Give the position of every Plasmodium parasite.
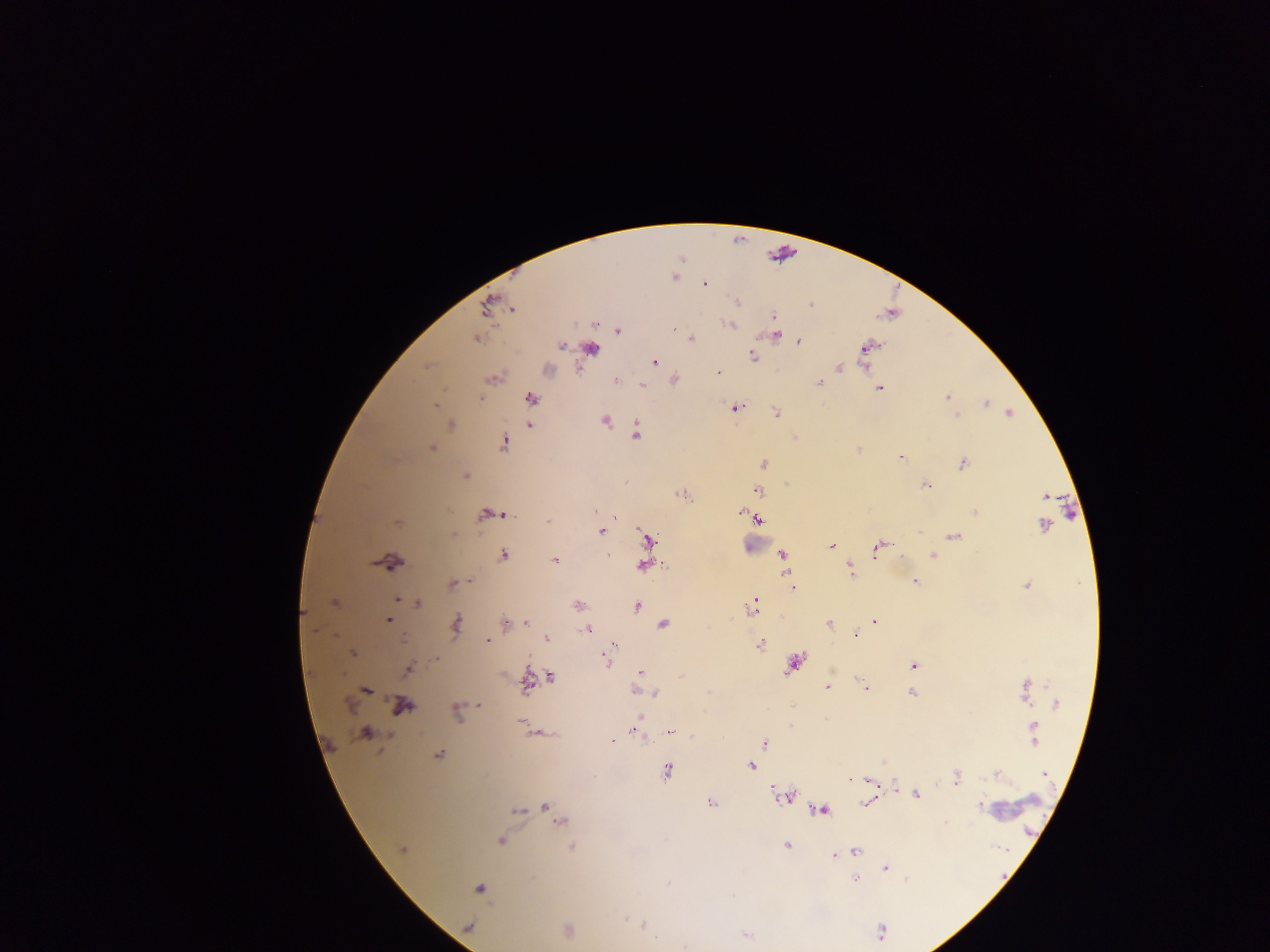

Approximate centers as {x, y} in pixels.
Plasmodium parasites: {703, 283}, {736, 304}, {812, 308}, {773, 315}, {730, 326}, {673, 327}, {775, 334}, {691, 338}, {477, 339}, {796, 339}, {798, 342}, {561, 345}, {865, 347}, {590, 348}, {861, 354}, {753, 355}, {654, 362}, {865, 364}, {839, 368}, {719, 373}, {614, 379}, {818, 383}, {642, 385}, {879, 388}, {946, 397}, {480, 398}, {530, 398}, {987, 403}, {435, 405}, {735, 408}, {776, 413}, {1009, 413}, {952, 414}, {957, 414}, {606, 420}, {528, 424}, {637, 434}, {504, 440}, {432, 448}, {858, 448}, {900, 456}, {764, 463}, {962, 464}, {465, 475}, {926, 484}, {757, 490}, {1044, 496}, {595, 510}, {740, 512}, {973, 512}, {482, 513}, {504, 515}, {548, 519}, {758, 519}, {1042, 526}, {599, 531}, {920, 532}, {953, 536}, {646, 538}, {832, 546}, {877, 549}, {608, 553}, {503, 554}, {782, 554}, {932, 554}, {554, 560}, {388, 563}, {642, 566}, {850, 567}, {787, 575}, {916, 581}, {451, 582}, {469, 582}, {1025, 585}, {794, 590}, {397, 600}, {417, 603}, {576, 605}, {754, 606}, {638, 607}, {749, 610}, {304, 613}, {388, 620}, {875, 621}, {503, 622}, {527, 624}, {662, 624}, {829, 624}, {455, 625}, {588, 629}, {855, 635}, {546, 638}, {486, 640}, {761, 645}, {352, 654}, {606, 660}, {912, 665}, {407, 669}, {832, 669}, {640, 672}, {527, 675}, {639, 675}, {552, 676}, {680, 677}, {526, 684}, {1024, 685}, {866, 686}, {828, 687}, {367, 690}, {634, 691}, {655, 692}, {910, 692}, {1026, 701}, {480, 704}, {791, 705}, {399, 706}, {455, 708}, {638, 716}, {520, 721}, {790, 725}, {1034, 725}, {634, 729}, {366, 732}, {671, 733}, {636, 734}, {612, 740}, {1037, 740}, {1035, 742}, {765, 743}, {438, 754}, {883, 760}, {752, 767}, {667, 771}, {1042, 773}, {996, 776}, {957, 777}, {865, 781}, {872, 784}, {897, 789}, {915, 795}, {784, 797}, {709, 802}, {543, 804}, {862, 806}, {978, 806}, {514, 811}, {821, 811}, {560, 822}, {946, 822}, {500, 841}, {786, 845}, {571, 847}, {402, 851}, {856, 852}, {833, 855}, {886, 867}, {854, 878}, {906, 879}, {669, 884}, {478, 888}, {644, 925}, {566, 930}, {882, 932}, {747, 936}.

field_of_view: single
country: Ghana
image_size: 1270×952 pixels
preparation: thick blood smear
capture: mobile-phone photograph through a microscope